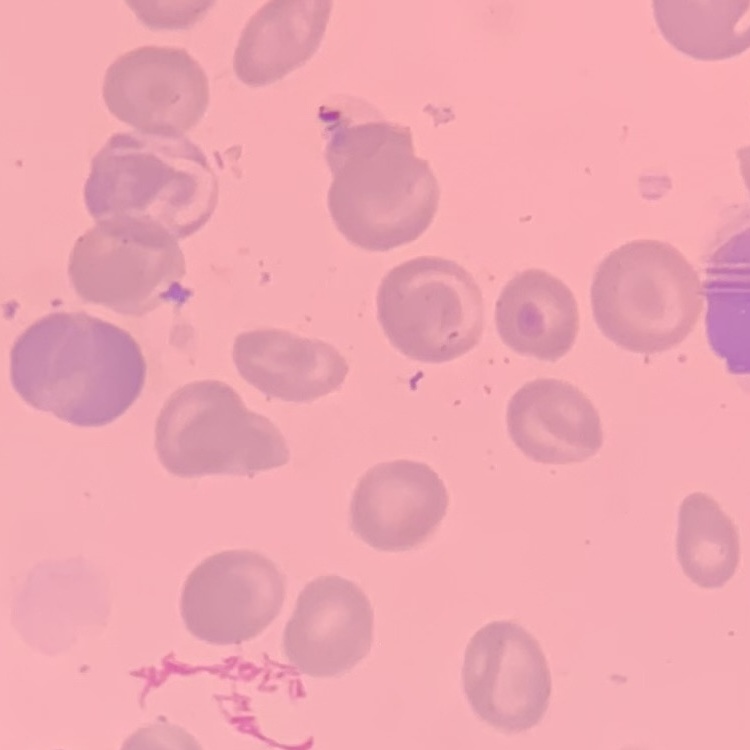
erythrocyte morphology = no rouleaux formation
stain = Field's or Giemsa
image type = square crop of a larger photomicrograph
preparation = thin peripheral smear